State which parasite is depicted.
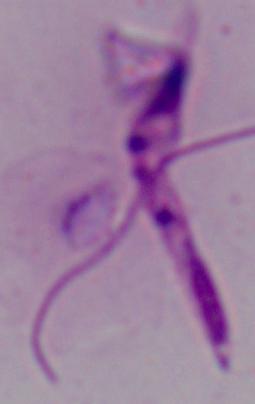
Leishmania.

Captured at 1000x magnification. Photomicrograph.